Locate every blood parasite and identify its species.
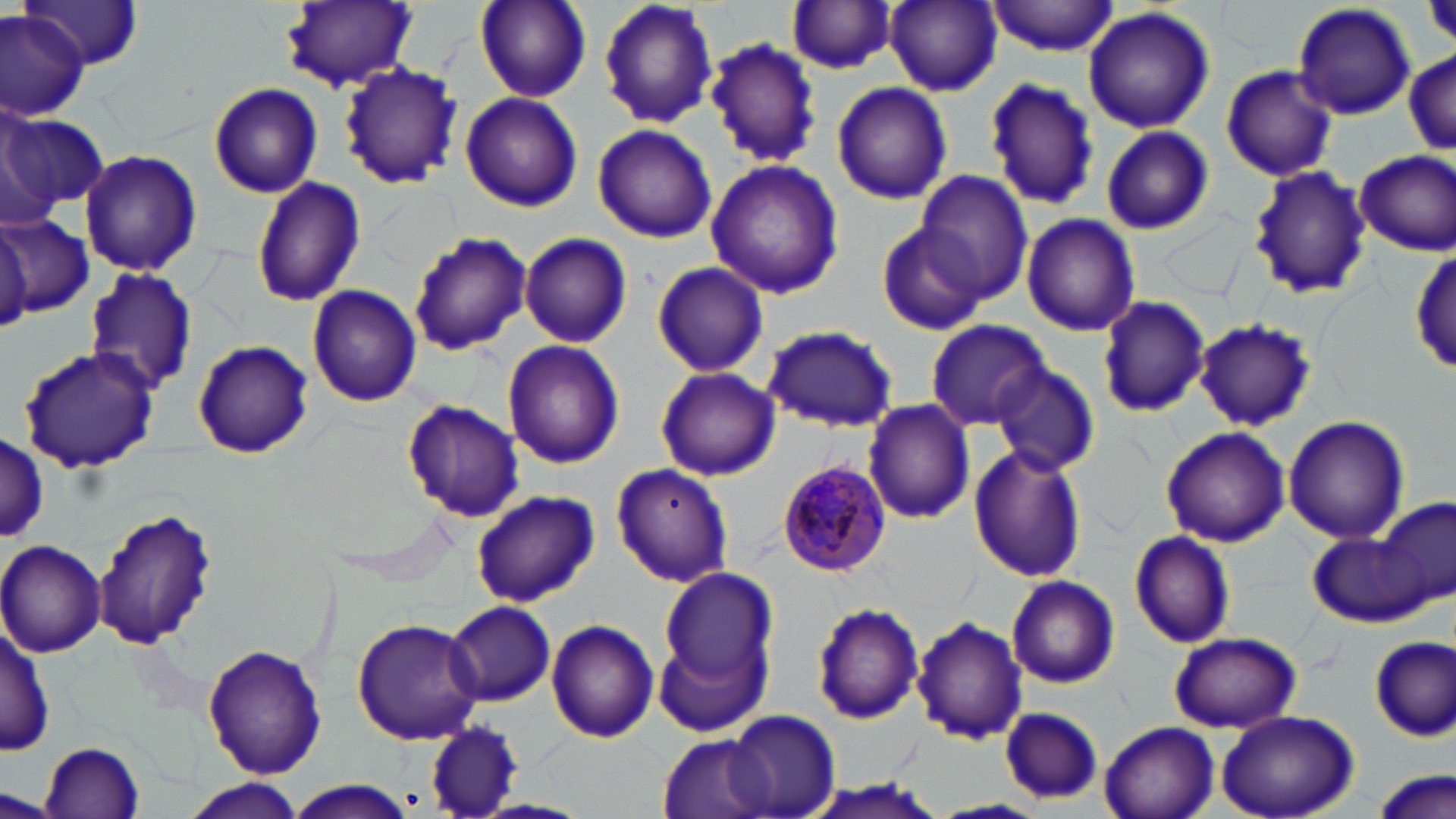
Approximate bounding boxes as (x1,y1)-(x2,y2) corner pairs in pixels.
Plasmodium malariae-infected red blood cells: (773,458)-(891,579).
No Plasmodium falciparum, Plasmodium ovale, Plasmodium vivax, Babesia divergens, or Trypanosoma brucei observed.

Uninfected red blood cell locations: (474,0)-(592,102), (597,0)-(721,131), (986,0)-(1121,57), (19,1)-(145,71), (283,1)-(418,92), (787,1)-(900,75), (884,1)-(1002,96), (1290,2)-(1417,120), (1082,7)-(1215,135), (0,9)-(88,119), (706,37)-(823,168), (1403,49)-(1454,163), (338,62)-(464,190), (1218,63)-(1339,183), (981,80)-(1100,212), (831,81)-(953,206), (208,82)-(323,198), (459,93)-(583,213), (1,112)-(112,212), (0,120)-(60,230), (592,124)-(717,243), (1099,125)-(1214,236), (78,149)-(202,277), (1355,150)-(1455,256), (704,159)-(845,300), (1247,164)-(1373,300), (917,173)-(1032,302), (250,175)-(367,307), (1021,213)-(1141,337), (1,215)-(93,318), (0,220)-(31,332), (875,220)-(989,336), (407,231)-(533,357), (519,231)-(632,348), (1409,242)-(1455,379), (651,261)-(769,378), (82,266)-(198,395), (307,283)-(423,406), (1096,295)-(1210,419), (925,319)-(1050,429), (1193,319)-(1316,431), (762,325)-(899,432), (192,339)-(313,459), (501,339)-(626,469), (18,349)-(160,472), (991,361)-(1100,476), (655,365)-(780,481), (403,399)-(522,523), (864,400)-(975,523), (1282,415)-(1410,545), (1159,426)-(1290,547), (1,436)-(49,541), (967,444)-(1089,583), (610,463)-(734,588), (471,489)-(599,607), (1372,497)-(1454,613), (90,507)-(217,652), (1127,529)-(1236,649), (1307,530)-(1431,629), (0,539)-(107,657), (660,569)-(780,695), (1005,573)-(1121,690), (444,600)-(557,707), (812,602)-(924,725), (913,615)-(1027,745), (350,617)-(484,744), (547,619)-(659,743), (652,619)-(773,743), (1,623)-(53,757), (1168,631)-(1303,732), (1371,635)-(1454,740), (201,643)-(327,778), (997,707)-(1103,799), (1216,708)-(1360,818), (726,710)-(841,817), (420,719)-(525,819), (1100,721)-(1219,819), (656,733)-(773,818), (39,741)-(147,817), (1372,767)-(1454,819), (180,779)-(308,817), (282,781)-(420,818). Slide-level diagnosis: Plasmodium malariae. Captured at 1000x magnification. May-Grünwald-Giemsa-stained preparation. Light microscopy. Thin blood film. Image is 1456×819 pixels. One field of a larger specimen.